Comment on the morphology of the erythrocytes.
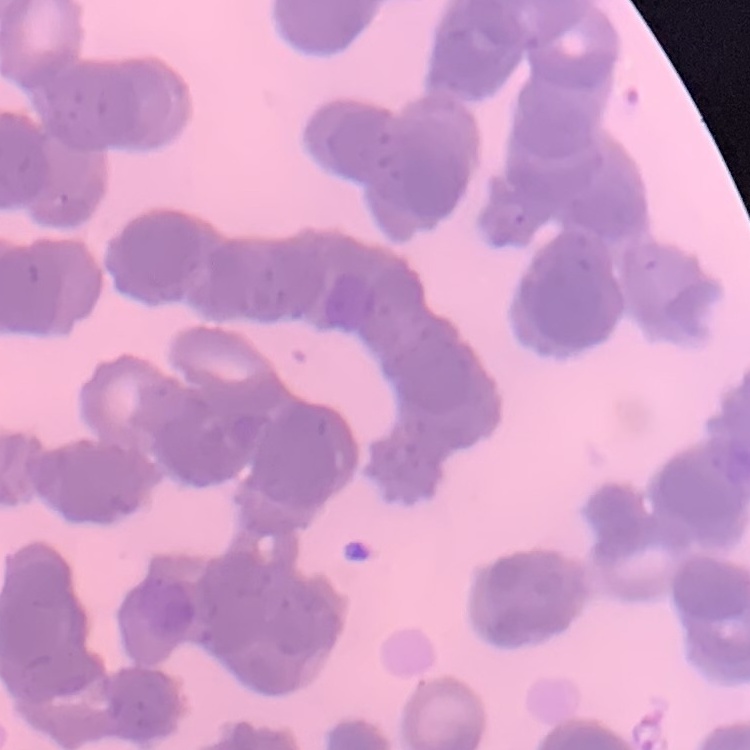

Rouleaux formation.

stain = Field's or Giemsa
preparation = thin blood film
image type = one tile cut from a larger photomicrograph